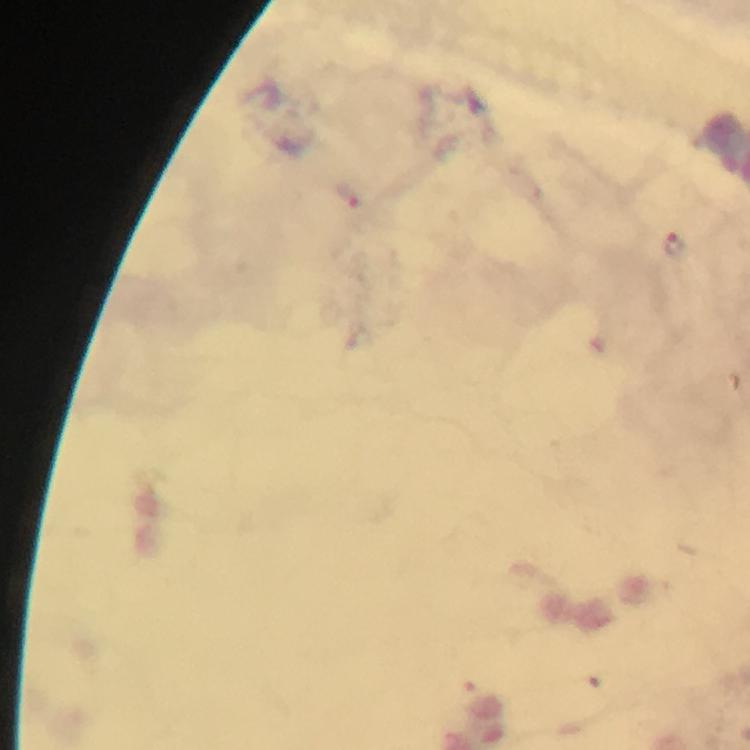
Approximate object centers, in pixels from the top-left corner.
Summary:
  - Malaria parasite locations: (x=675, y=243)
  - Context: from a malaria diagnostic workup
  - Immersion oil: used
  - Cropped from: a single field of view
  - Magnification: 100x
  - Preparation: thick blood film
  - Image size: 750×750 pixels
  - Capture: smartphone mounted on the microscope
  - Stain: Giemsa